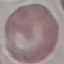
malaria status = uninfected
capture = smartphone camera at the microscope eyepiece
image type = automatically extracted cell patch, resized to 64 × 64 pixels
stain = Giemsa
preparation = thin smear